Report the malaria status of this cell.
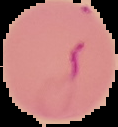
Parasitized.

image size = 118×127 pixels
preparation = thin blood smear
image type = segmented cell region with the area outside set to black